Comment on the morphology of the erythrocytes.
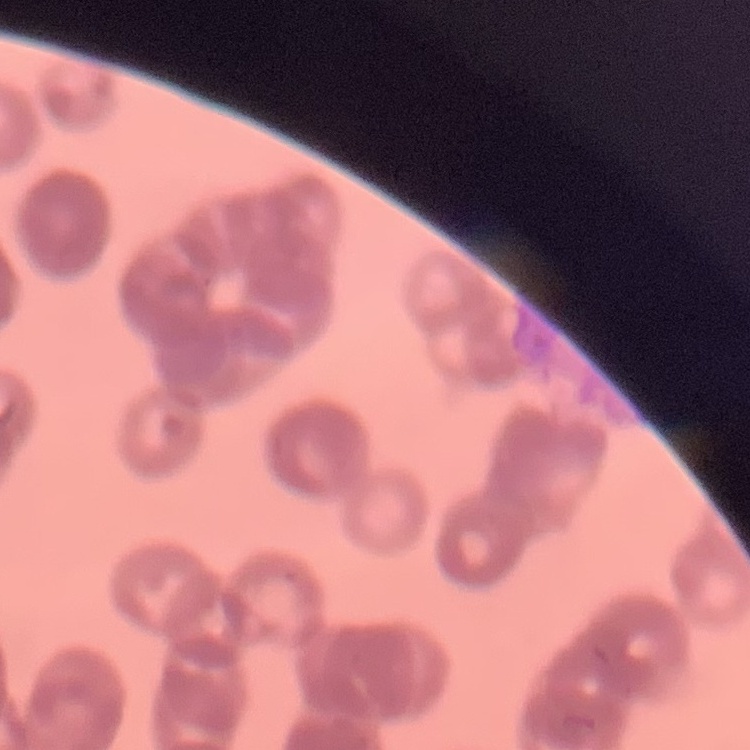

Rouleaux formation.

Summary:
  - Stain: Field's or Giemsa
  - Image type: square crop of a larger photomicrograph
  - Preparation: thin blood film